Identify the blood parasite species.
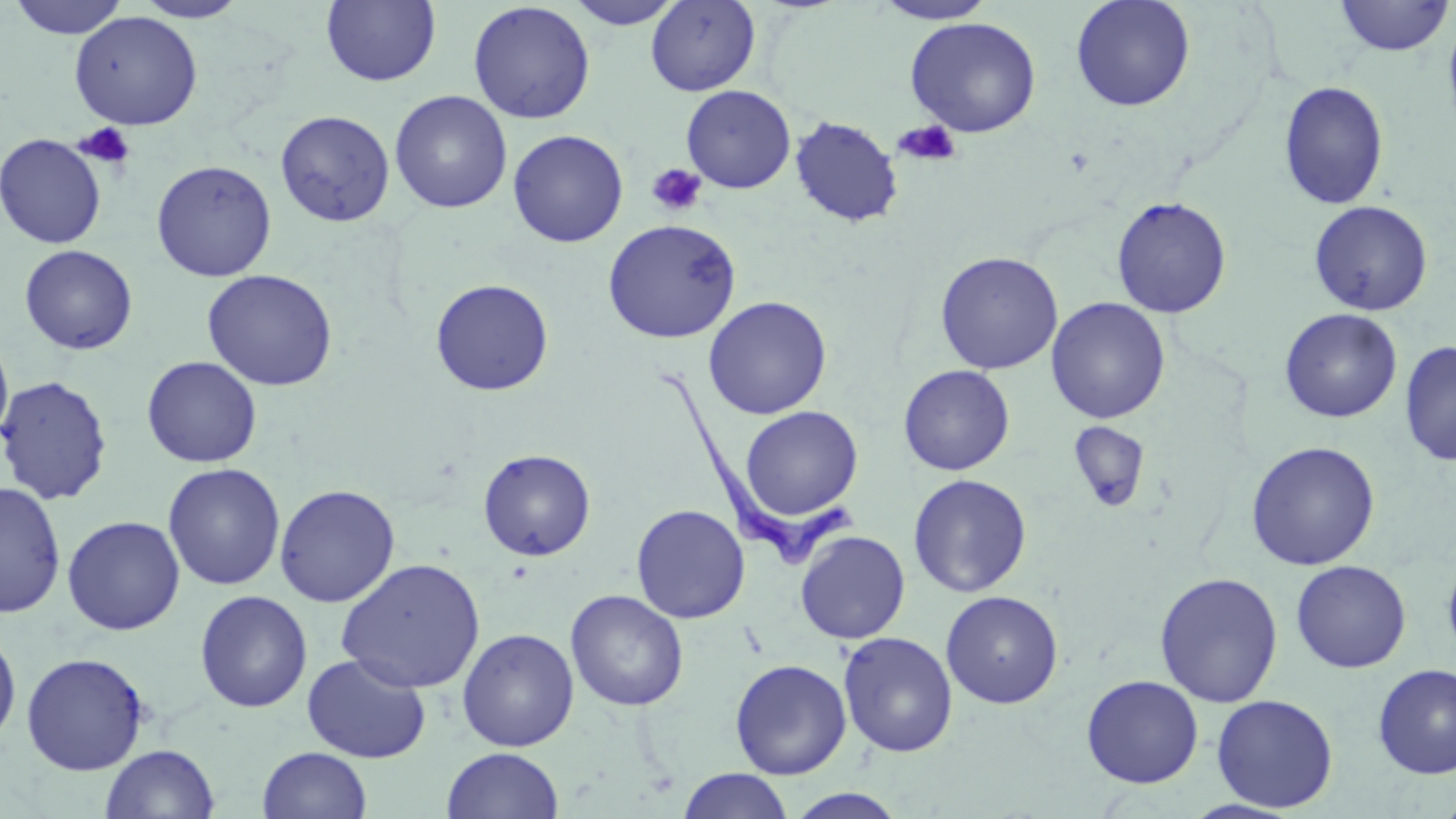
Trypanosoma brucei.

Summary:
  - Coordinate format: approximate bounding boxes as [x1, y1, x2, y2] in pixels
  - Platelet locations: [893, 120, 961, 167], [74, 122, 136, 170], [646, 163, 707, 217]
  - Uninfected red blood cell locations: [6, 0, 131, 39], [320, 0, 441, 87], [564, 0, 685, 29], [646, 0, 760, 96], [872, 0, 998, 24], [1070, 0, 1195, 112], [1334, 0, 1453, 57], [132, 1, 249, 23], [468, 2, 595, 124], [69, 11, 203, 130], [1442, 13, 1456, 144], [905, 16, 1041, 138], [1278, 81, 1389, 211], [681, 85, 796, 194], [389, 90, 512, 214], [275, 110, 395, 227], [790, 116, 903, 227], [507, 129, 629, 247], [0, 133, 107, 249], [151, 160, 277, 282], [1111, 195, 1232, 319], [1308, 200, 1433, 316], [601, 218, 741, 344], [19, 244, 138, 355], [934, 251, 1063, 375], [202, 269, 338, 391], [430, 278, 554, 396], [703, 296, 832, 420], [1045, 297, 1170, 424], [1279, 308, 1402, 423], [0, 330, 14, 450], [1400, 340, 1456, 467], [142, 355, 262, 468], [898, 365, 1015, 475], [0, 375, 113, 505], [740, 406, 863, 521], [1069, 421, 1150, 511], [1245, 441, 1380, 570], [478, 449, 596, 561], [163, 463, 286, 591], [908, 473, 1032, 598], [0, 481, 66, 618], [274, 484, 400, 607], [631, 504, 750, 624], [62, 515, 186, 635], [795, 530, 911, 644], [1442, 551, 1456, 664], [336, 558, 485, 693], [1291, 560, 1411, 673], [1154, 571, 1284, 708], [565, 589, 689, 711], [194, 590, 312, 713], [941, 590, 1064, 709], [0, 628, 22, 749], [457, 628, 579, 751], [838, 631, 958, 757], [21, 652, 149, 775], [301, 652, 432, 764], [729, 659, 852, 779], [1372, 663, 1456, 779], [1081, 675, 1204, 789], [1211, 694, 1339, 812], [100, 743, 220, 819], [257, 746, 373, 819], [442, 747, 564, 819], [677, 769, 794, 819], [785, 788, 910, 818]
  - Trypanosoma brucei locations: [658, 366, 858, 567]
  - Magnification: 1000x
  - Modality: light microscopy
  - Stain: May-Grünwald-Giemsa
  - Preparation: thin blood smear
  - Image size: 1456×819 pixels
  - Field of view: one of a larger specimen